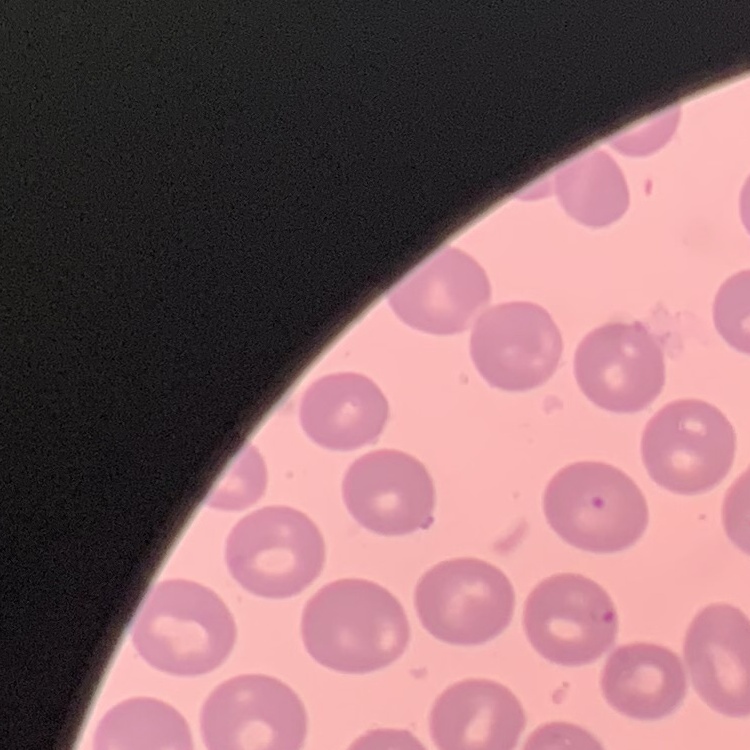

The red blood cells show no rouleaux formation. Field's or Giemsa stain. Thin peripheral smear. Square crop of a larger photomicrograph.